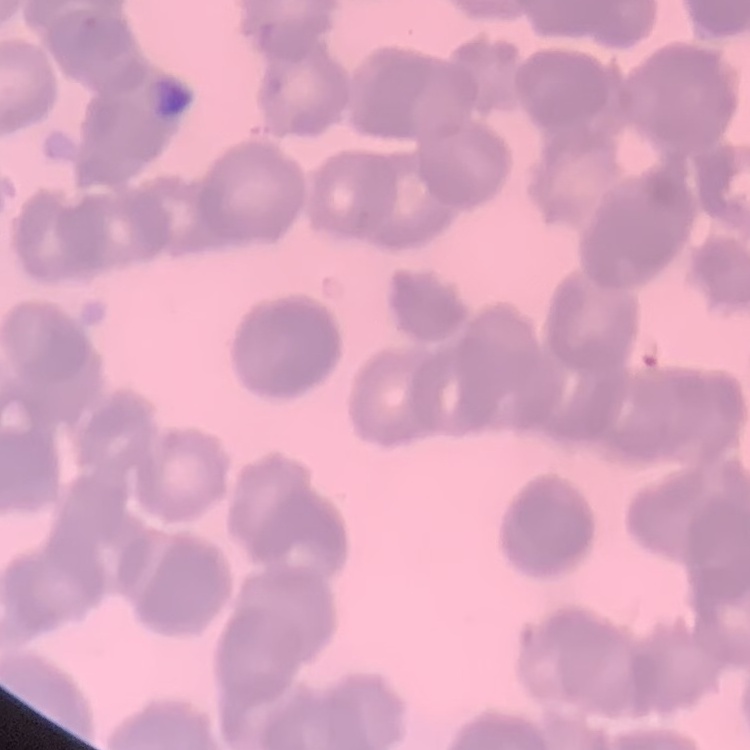
The red blood cells exhibit rouleaux formation. Field's or Giemsa stain. Thin blood smear. Square crop of a larger photomicrograph.